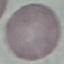

malaria status = uninfected
preparation = thin blood film
stain = Giemsa
image type = automatically extracted cell patch, resized to 64 × 64 pixels
capture = smartphone through the microscope eyepiece